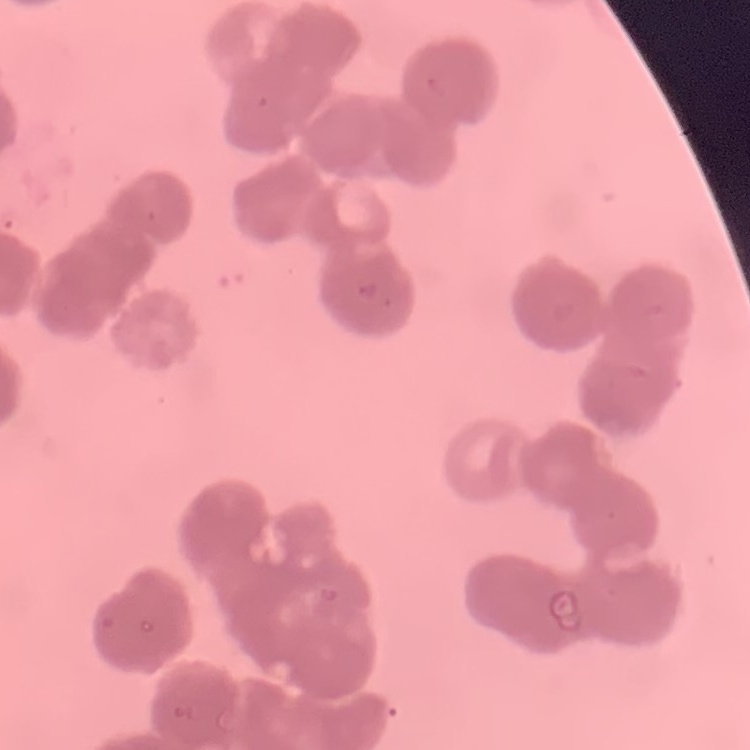
erythrocyte morphology = rouleaux formation
preparation = thin peripheral smear
image type = square crop of a larger photomicrograph
stain = Field's or Giemsa